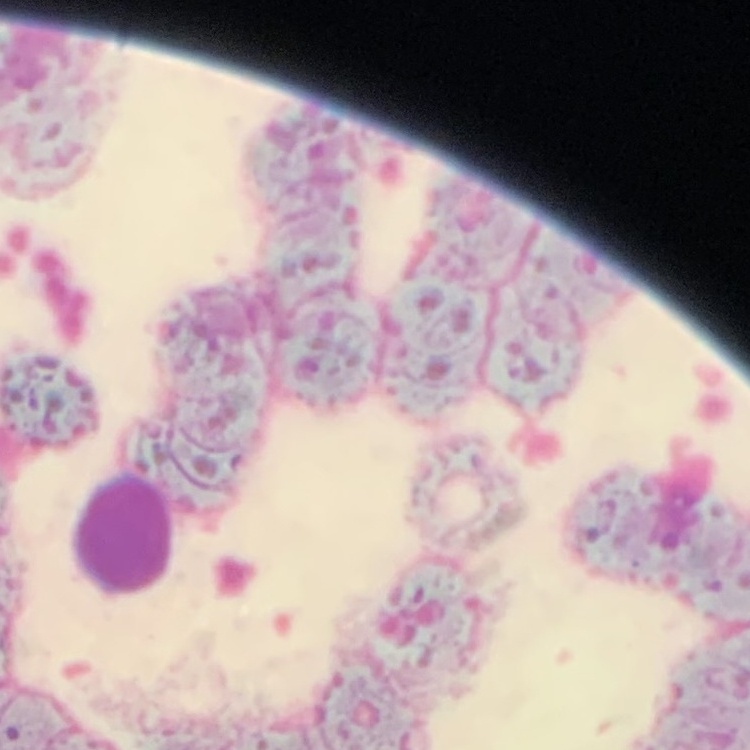

Summary:
  - Erythrocyte morphology: rouleaux formation
  - Image type: square crop of a larger photomicrograph
  - Preparation: thin blood smear
  - Stain: Field's or Giemsa